Assess this cell for malaria.
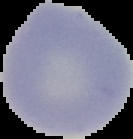
Uninfected.

Cell region segmented out of the field of view; the surrounding area is masked to black. Image is 133×139 pixels. From a thin blood film.